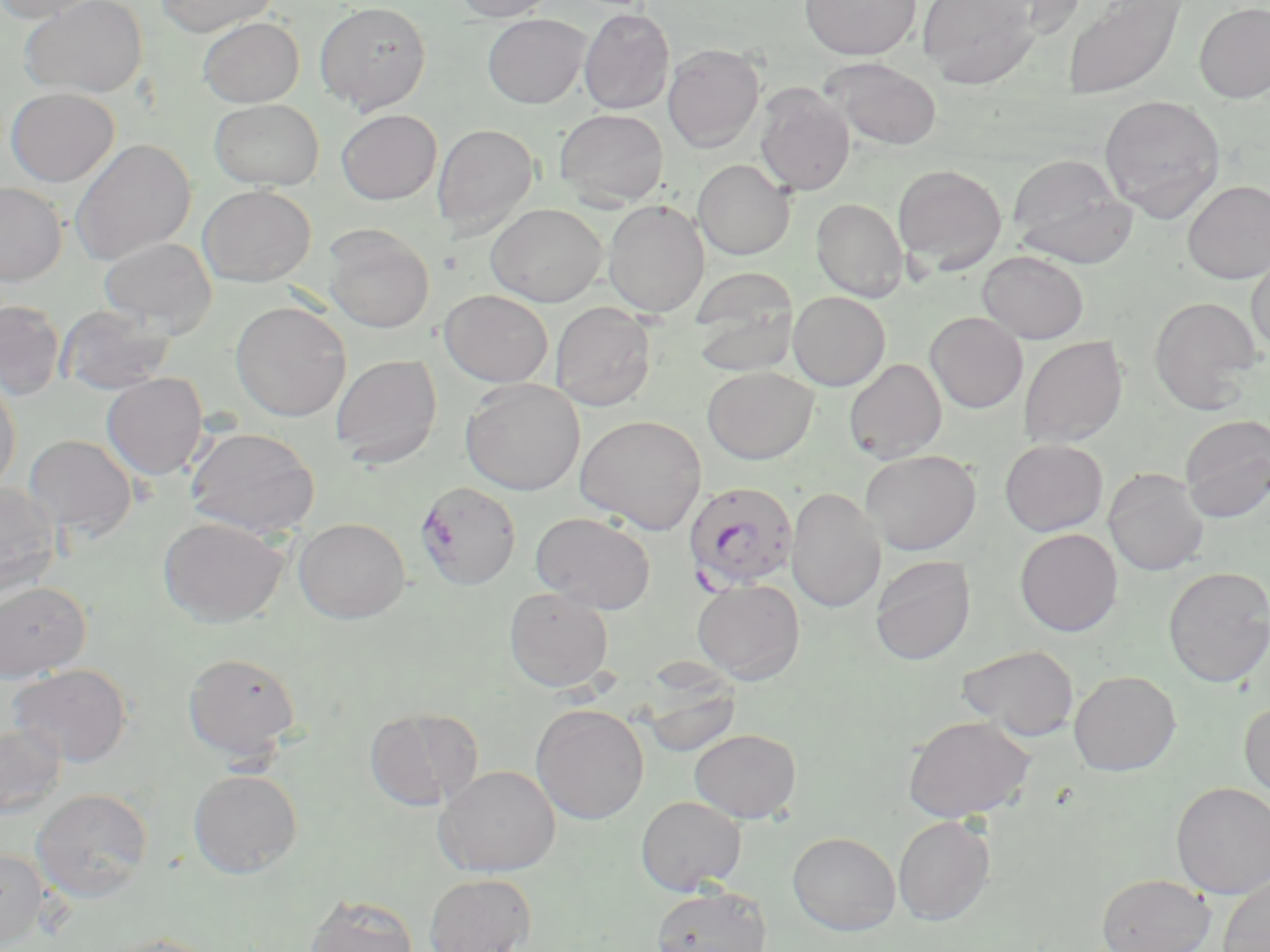

Approximate bounding boxes as (x1, y1, x2, y2) in pixels. Uninfected red blood cell locations: (0, 0, 103, 23), (20, 0, 148, 99), (157, 0, 278, 36), (454, 0, 558, 21), (800, 0, 920, 60), (917, 0, 1040, 88), (979, 0, 1086, 37), (1062, 0, 1185, 98), (315, 2, 431, 114), (1194, 3, 1270, 103), (578, 7, 675, 114), (482, 14, 590, 108), (198, 17, 304, 107), (663, 43, 764, 152), (823, 58, 942, 150), (754, 84, 856, 197), (5, 87, 119, 187), (1100, 94, 1225, 221), (209, 99, 324, 190), (554, 108, 668, 208), (336, 109, 441, 204), (432, 123, 538, 237), (70, 138, 196, 265), (1007, 154, 1137, 268), (693, 159, 795, 260), (892, 164, 1007, 274), (1183, 180, 1270, 284), (0, 182, 67, 285), (198, 184, 315, 286), (811, 198, 908, 301), (602, 199, 710, 318), (486, 203, 607, 306), (323, 226, 435, 333), (100, 237, 217, 334), (977, 250, 1089, 343), (1247, 251, 1270, 357), (689, 270, 800, 375), (439, 289, 553, 387), (787, 291, 890, 390), (1148, 296, 1263, 413), (0, 299, 67, 400), (230, 300, 351, 421), (549, 302, 657, 411), (56, 305, 176, 395), (925, 312, 1028, 413), (1019, 336, 1128, 448), (330, 354, 443, 467), (844, 358, 947, 464), (702, 366, 819, 464), (101, 373, 208, 480), (0, 375, 21, 496), (461, 378, 585, 495), (574, 413, 707, 534), (1179, 414, 1270, 523), (184, 425, 320, 537), (22, 434, 137, 541), (999, 439, 1108, 536), (860, 450, 981, 555), (1104, 468, 1208, 575), (0, 481, 61, 599), (787, 486, 885, 613), (530, 512, 656, 612), (158, 517, 288, 627), (293, 517, 410, 623), (1014, 528, 1123, 636), (870, 555, 975, 665), (1163, 566, 1270, 687), (691, 579, 805, 683), (0, 581, 91, 681), (503, 587, 614, 692), (956, 644, 1079, 740), (183, 652, 301, 760), (9, 664, 133, 767), (1068, 670, 1180, 775), (643, 680, 740, 759), (1239, 699, 1270, 800), (531, 703, 649, 824), (364, 706, 482, 812), (902, 715, 1036, 822), (0, 723, 67, 819), (689, 728, 801, 823), (435, 765, 560, 877), (188, 768, 303, 878), (1170, 782, 1270, 898), (31, 788, 153, 902), (636, 795, 747, 895), (893, 815, 996, 925), (787, 831, 900, 935), (0, 848, 49, 946), (424, 873, 536, 952), (1096, 873, 1216, 952), (1218, 873, 1270, 952), (650, 884, 773, 952), (303, 893, 419, 952), (101, 933, 220, 952). Plasmodium falciparum-infected red blood cell locations: (415, 481, 521, 590), (682, 481, 799, 591). Slide-level diagnosis: Plasmodium falciparum. Optical microscopy. May-Grünwald-Giemsa-stained preparation. One field of a larger specimen. 1000x magnification. Thin blood film. Image is 1270×952 pixels.